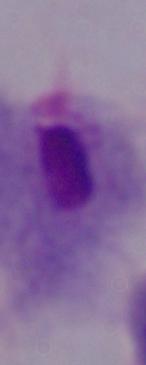
Summary:
  - Modality: photomicrograph
  - Identification: trichomonad
  - Magnification: 1000x